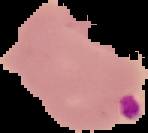
image_size: 148×133 pixels
result: Plasmodium parasites detected
preparation: thin blood smear
image_type: segmented cell region with the area outside set to black